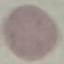
malaria status = uninfected
capture = smartphone through the microscope eyepiece
stain = Giemsa
preparation = thin blood film
image type = automatically extracted cell patch, resized to 64 × 64 pixels